Give the position of every malaria parasite.
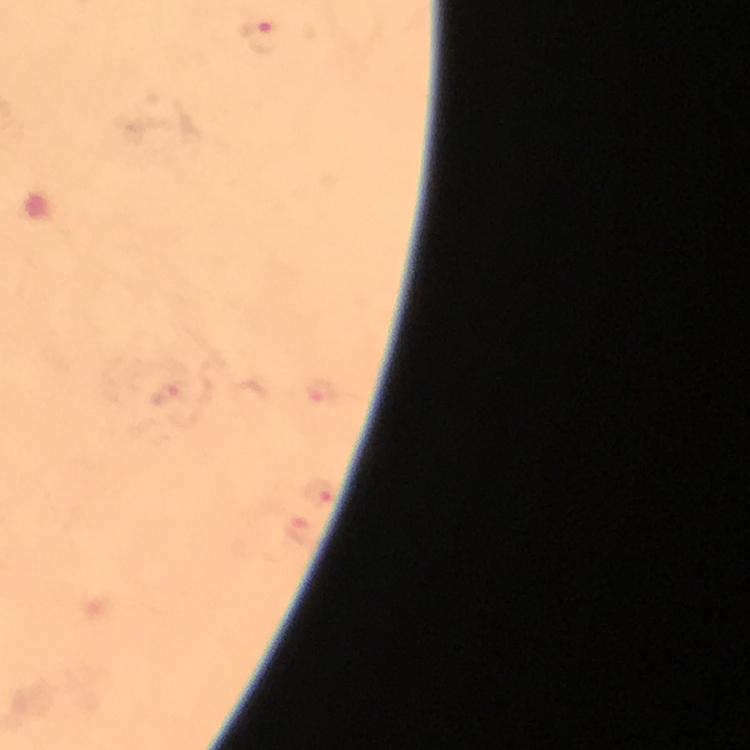
Approximate object centers, in pixels from the top-left corner.
Malaria parasites: (x=258, y=36), (x=319, y=392), (x=168, y=396), (x=318, y=492), (x=296, y=529).

immersion oil = applied
cropped from = a single field of view
magnification = 100x
context = from a malaria diagnostic workup
stain = Giemsa
preparation = thick blood film
image size = 750×750 pixels
capture = smartphone photograph through a microscope